Classify this cell by malaria status.
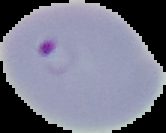

It is parasitized.

preparation: thin blood film
image_type: cell region segmented out of the field of view; surrounding area masked to black
image_size: 166×133 pixels